Comment on the morphology of the red blood cells.
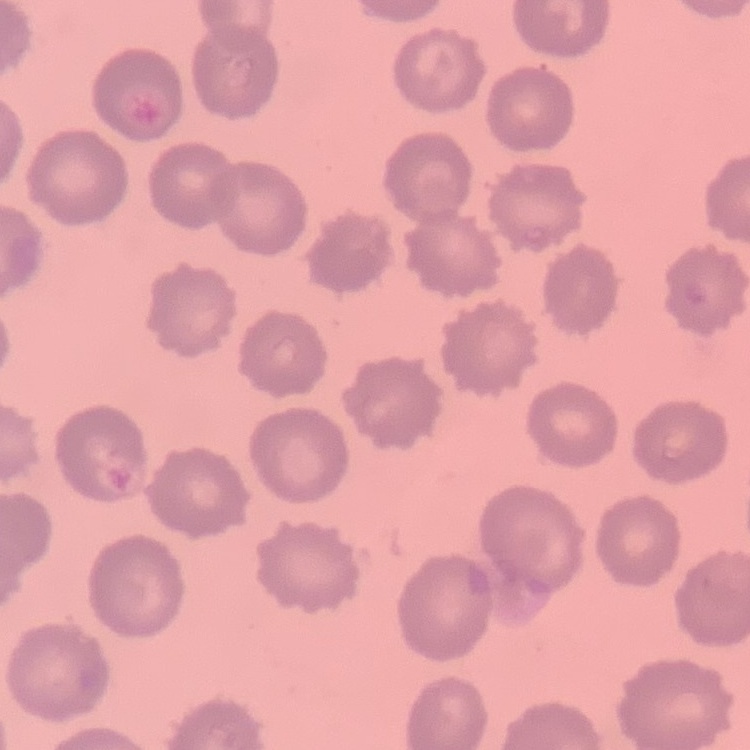

They show no rouleaux formation.

Summary:
  - Image type: square crop of a larger photomicrograph
  - Stain: Field's or Giemsa
  - Preparation: thin blood film